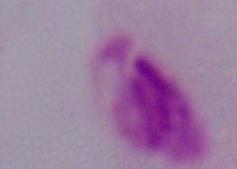

{
  "identification": "trichomonad",
  "modality": "photomicrograph",
  "magnification": "1000x"
}